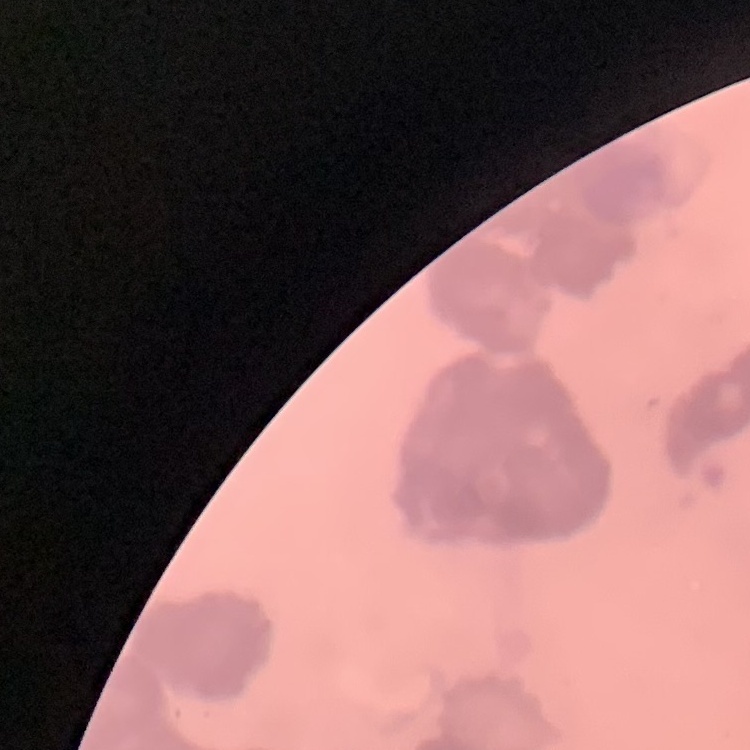
red blood cell morphology = rouleaux formation
preparation = thin blood smear
stain = Field's or Giemsa
image type = one tile cut from a larger photomicrograph